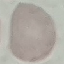

Summary:
  - Result: negative for malaria parasites
  - Capture: smartphone camera at the microscope eyepiece
  - Image type: cell patch, automatically extracted from a larger field of view and resized to 64 × 64 pixels
  - Preparation: thin blood film
  - Stain: Giemsa